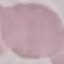
Malaria status: uninfected. Giemsa stain. Automatically extracted cell patch, resized to 64 × 64 pixels. Thin blood film. Photographed with a smartphone camera at the microscope eyepiece.